State which cell type is depicted.
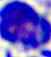

This is a leukocyte.

modality = photomicrograph
magnification = 400x